Assess this cell for malaria.
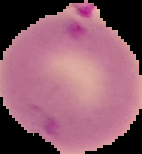

It is parasitized.

Summary:
  - Image type: cell region segmented out of the field of view; surrounding area masked to black
  - Preparation: thin blood film
  - Image size: 142×154 pixels